State which parasite is depicted.
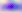

This is Toxoplasma gondii.

Photomicrograph. 400x magnification.